Report the malaria status of this cell.
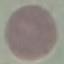
Uninfected.

Summary:
  - Preparation: thin smear
  - Stain: Giemsa
  - Capture: smartphone through the microscope eyepiece
  - Image type: cell patch, automatically extracted from a larger field of view and resized to 64 × 64 pixels